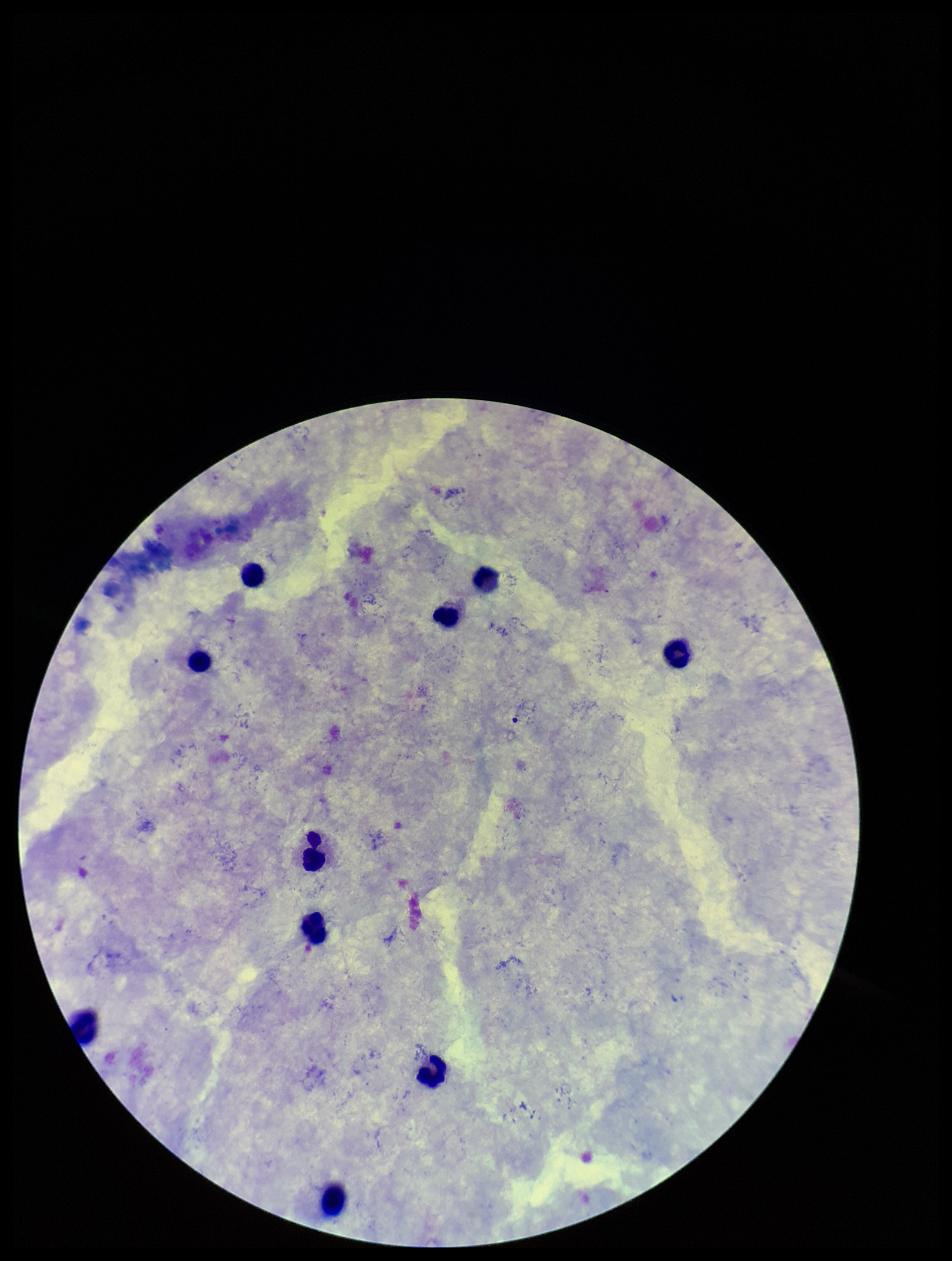
Parasite count: 0. Smartphone photograph taken through the eyepiece of a microscope. Leukocyte count: 10. Plasmodium parasites: none identified. Single field of view. Giemsa stain. Patient malaria status: negative. Preparation: thick smear. Image is 952×1261 pixels.